State the preparation type.
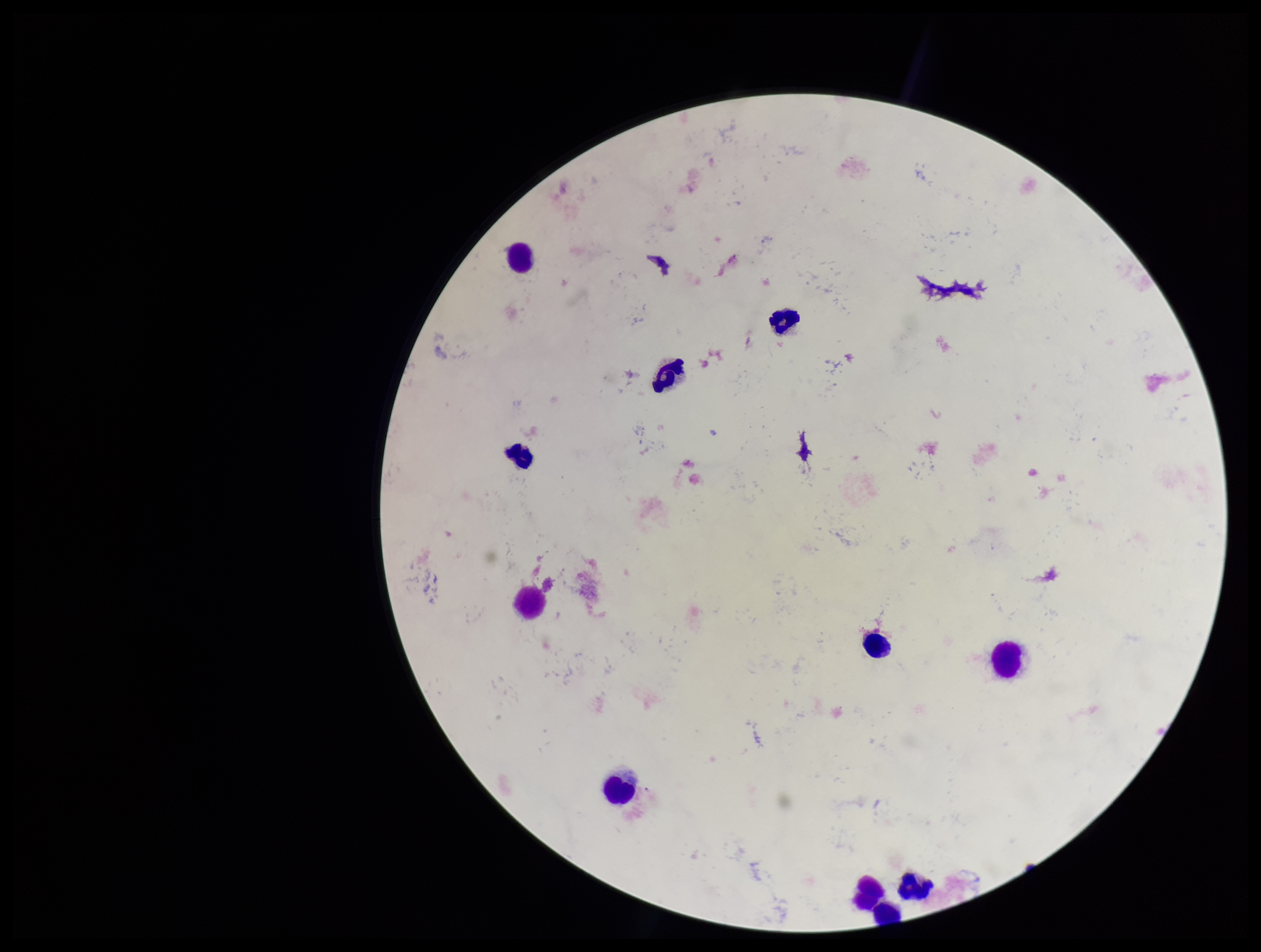
It is a thick blood smear.

Parasite count: 0. Leukocyte count: 10. Patient malaria status: negative. Plasmodium parasites: none seen. Stained with Giemsa. Photographed through the microscope eyepiece with a smartphone camera. One field from this slide. Image is 1261×952 pixels.